Report the malaria status of this cell.
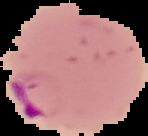
Parasitized.

Summary:
  - Image size: 148×136 pixels
  - Image type: segmented cell region on a black background
  - Preparation: thin blood film